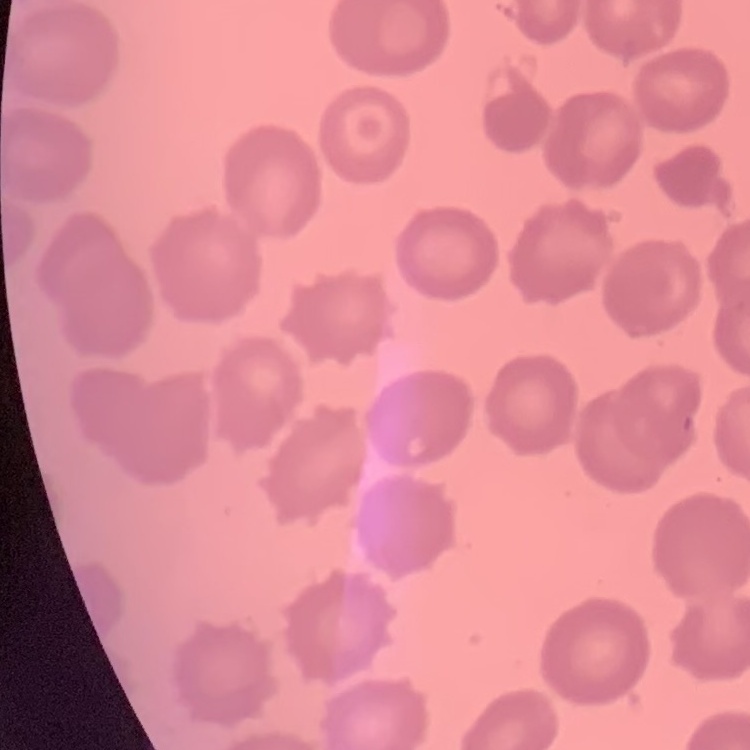

red blood cell morphology = no rouleaux formation
preparation = thin blood smear
image type = one tile cut from a larger photomicrograph
stain = Field's or Giemsa